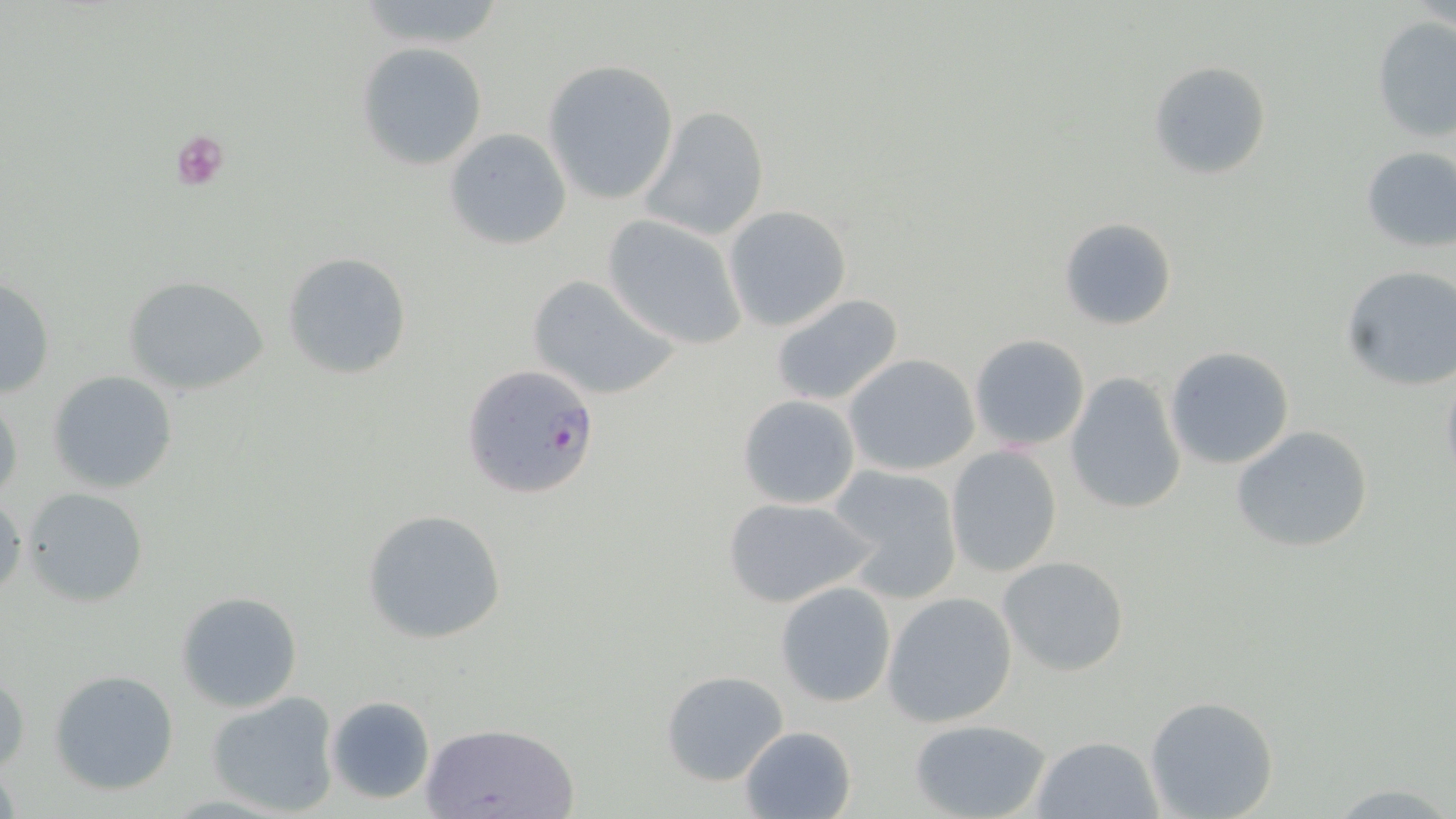

Approximate bounding boxes as [x1, y1, x2, y2] in pixels. Platelet locations: [170, 129, 232, 191]. Uninfected red blood cell locations: [1370, 16, 1456, 141], [357, 42, 489, 171], [542, 60, 679, 205], [1148, 60, 1272, 181], [640, 106, 770, 242], [442, 127, 572, 250], [1358, 145, 1456, 254], [723, 204, 852, 331], [602, 215, 747, 350], [1057, 216, 1177, 331], [282, 252, 413, 379], [1339, 265, 1456, 392], [525, 273, 681, 400], [122, 275, 270, 395], [0, 277, 54, 399], [769, 292, 905, 408], [968, 334, 1091, 453], [1163, 345, 1295, 469], [843, 353, 981, 477], [1439, 366, 1456, 490], [47, 369, 180, 495], [1064, 371, 1187, 516], [0, 393, 24, 507], [736, 394, 863, 511], [1231, 425, 1372, 554], [945, 446, 1065, 579], [828, 463, 964, 602], [21, 486, 150, 606], [0, 493, 26, 600], [721, 494, 877, 609], [361, 508, 508, 646], [998, 555, 1131, 676], [774, 581, 898, 708], [176, 591, 305, 713], [881, 591, 1019, 727], [1, 668, 29, 777], [48, 669, 180, 795], [659, 669, 790, 787], [207, 692, 341, 815], [325, 695, 435, 804], [1143, 696, 1280, 819], [907, 717, 1054, 819], [426, 720, 576, 818], [737, 725, 857, 819], [1031, 734, 1164, 819], [1334, 782, 1453, 815]. Plasmodium falciparum-infected red blood cell locations: [462, 365, 601, 498]. Slide-level diagnosis: Plasmodium falciparum. Image is 1456×819 pixels. 1000x magnification. May-Grünwald-Giemsa-stained preparation. Light microscopy. Thin blood smear. Single field of view.